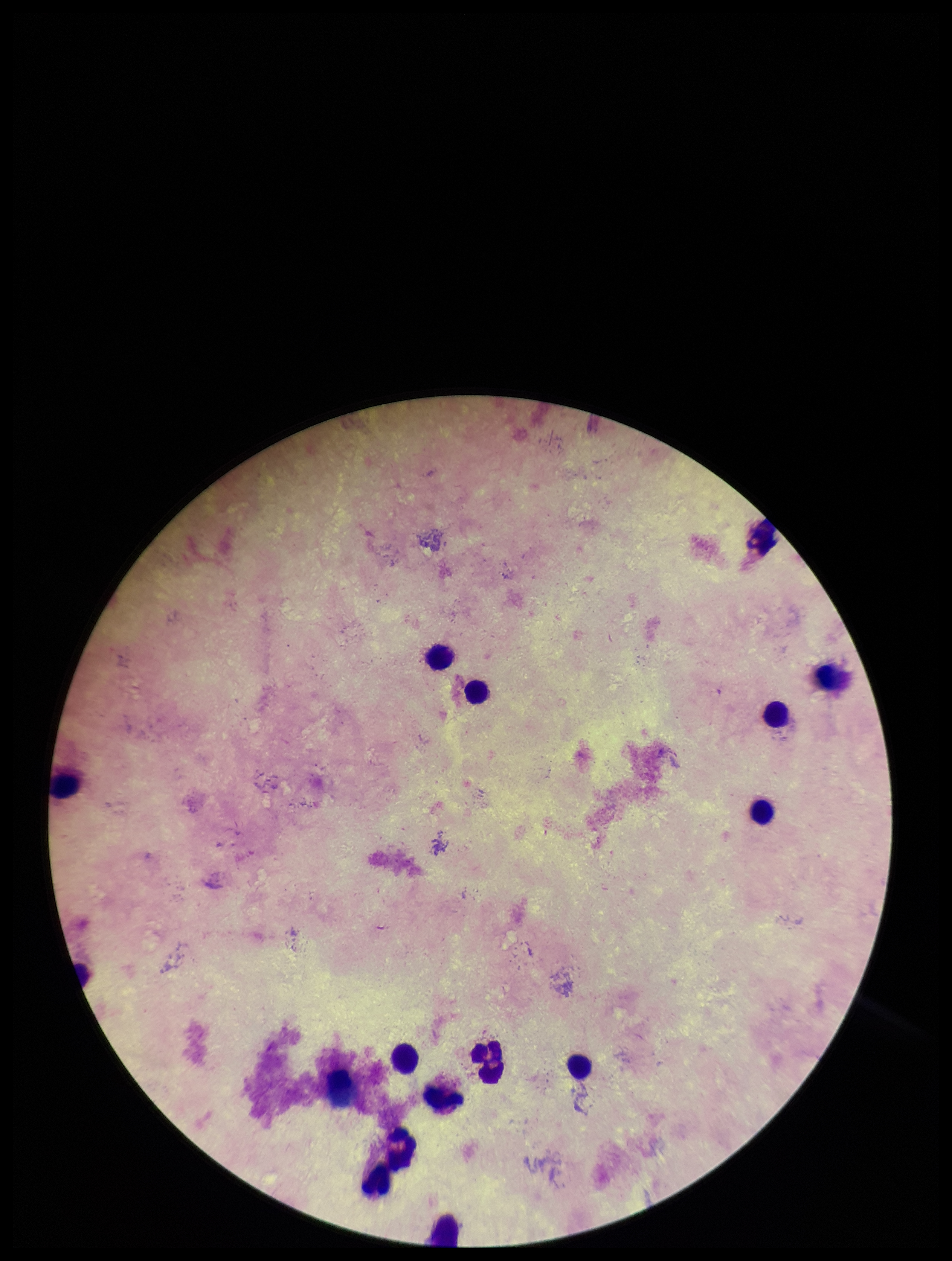

parasite count = 0
Plasmodium parasites = none seen
stain = Giemsa
field of view = single
patient malaria status = negative
preparation = thick blood smear
capture = smartphone photograph through the microscope eyepiece
leukocyte count = 15
image size = 952×1261 pixels